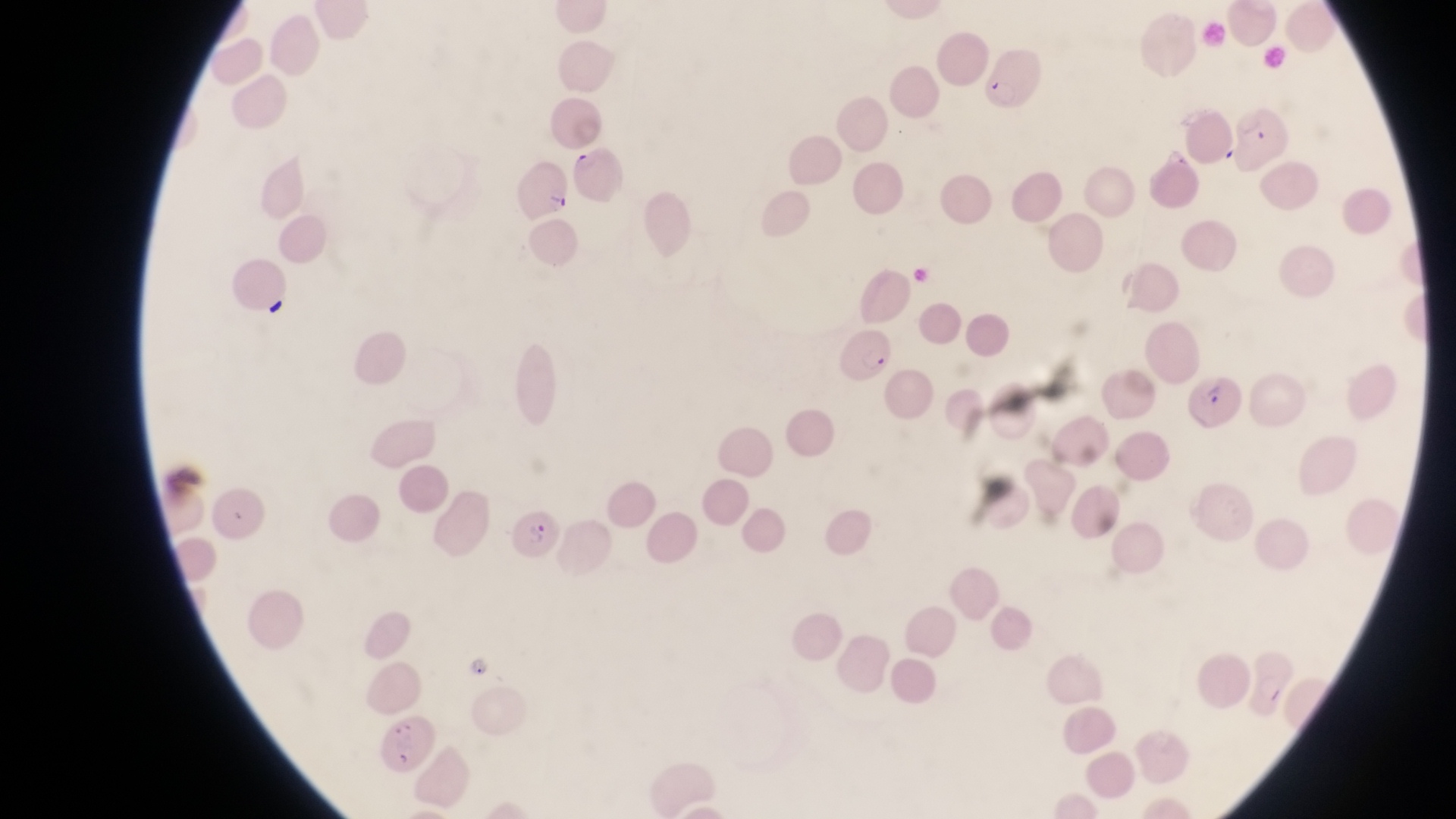

field of view = single
magnification = 1000x
artifact (platelet-like body, stain precipitate, or debris) locations = approximate bounding boxes as (left, top, right, bottom) in pixels: (261, 293, 293, 322)
capture = smartphone photograph through the eyepiece of an Olympus CX-23 microscope
parasitised red blood cell locations = approximate bounding boxes as (left, top, right, bottom) in pixels: (981, 46, 1042, 115), (1231, 105, 1292, 168), (566, 142, 625, 208), (507, 156, 571, 217), (832, 328, 896, 384), (1181, 364, 1241, 427), (515, 507, 565, 562)
image size = 1456×819 pixels
trophozoite locations = approximate bounding boxes as (left, top, right, bottom) in pixels: (1150, 143, 1192, 172), (465, 651, 495, 683)
country = Uganda
preparation = thin blood film